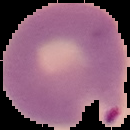

Summary:
  - Result: Plasmodium parasites identified
  - Preparation: thin blood film
  - Image type: segmented cell region on a black background
  - Image size: 130×130 pixels